Describe the morphology of the erythrocytes.
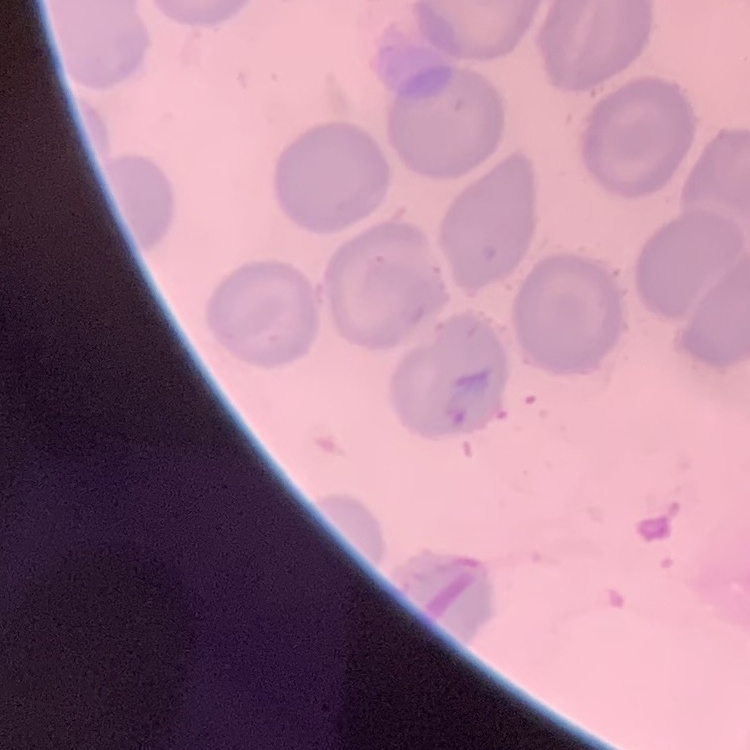

They show no rouleaux formation.

stain = Field's or Giemsa
image type = square crop of a larger photomicrograph
preparation = thin peripheral smear